Describe the morphology of the red blood cells.
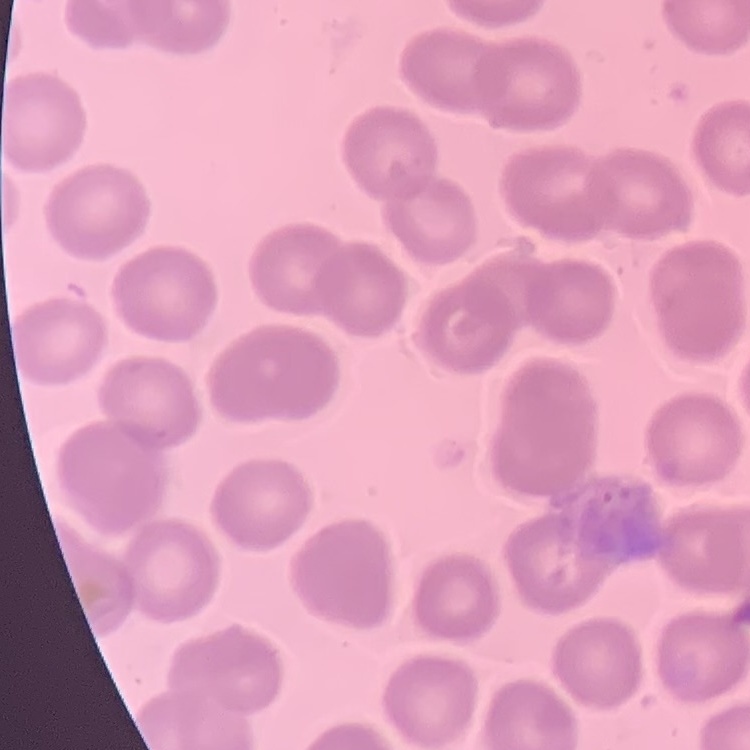

They show no rouleaux formation.

Summary:
  - Image type: one tile cut from a larger photomicrograph
  - Stain: Field's or Giemsa
  - Preparation: thin peripheral smear